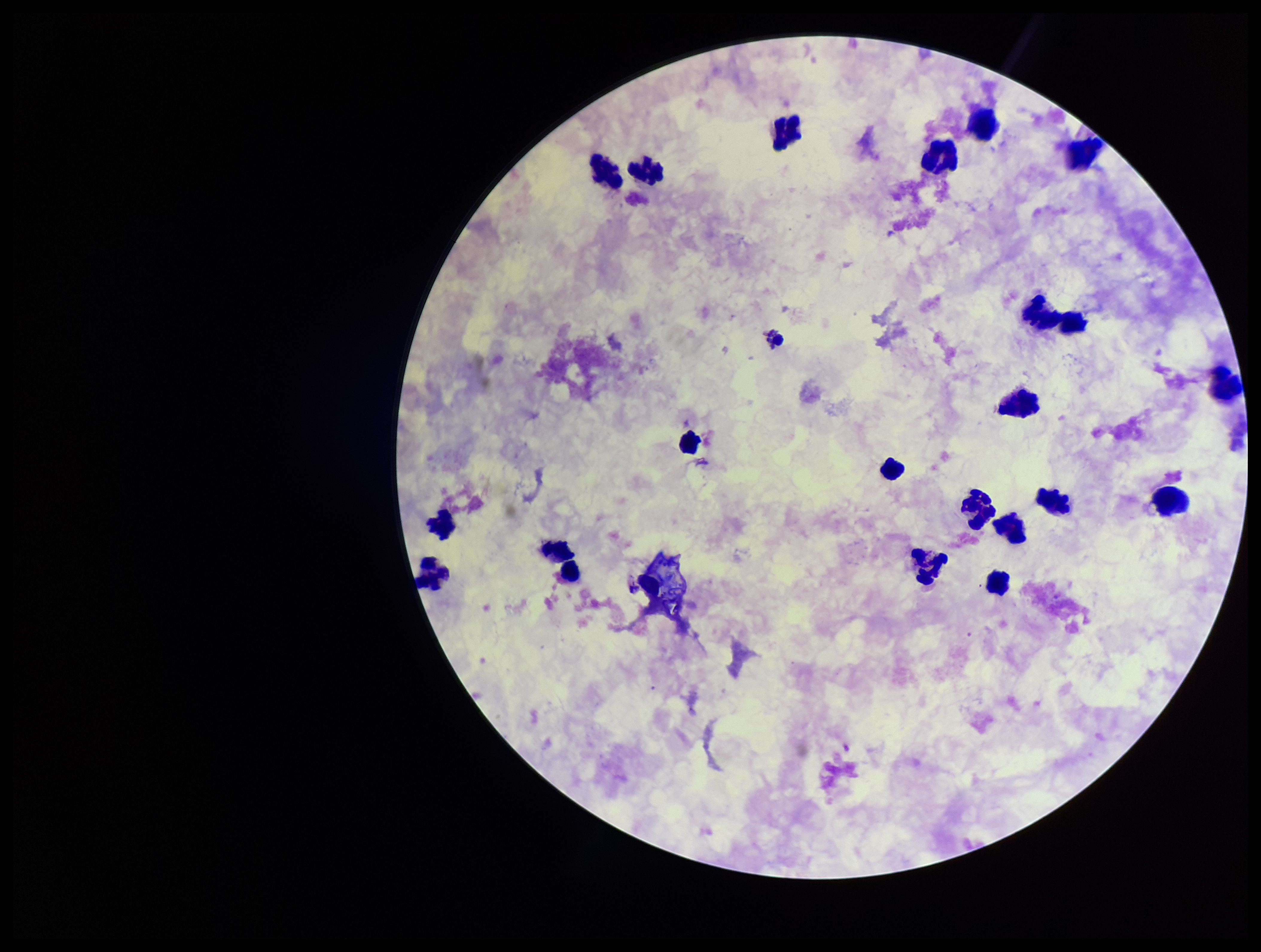

Summary:
  - Leukocyte count: 22
  - Parasite count: 0
  - Stain: Giemsa
  - Preparation: thick smear
  - Plasmodium parasites: none detected
  - Field of view: single
  - Image size: 1261×952 pixels
  - Capture: smartphone photograph through the microscope eyepiece
  - Patient malaria status: negative